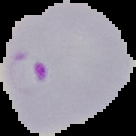
{
  "malaria_status": "parasitized",
  "image_size": "136×136 pixels",
  "preparation": "thin blood film",
  "image_type": "cell region segmented out of the field of view; surrounding area masked to black"
}